Assess this cell for malaria.
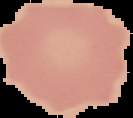
Uninfected.

preparation = thin blood smear
image type = segmented cell region with the area outside set to black
image size = 133×118 pixels